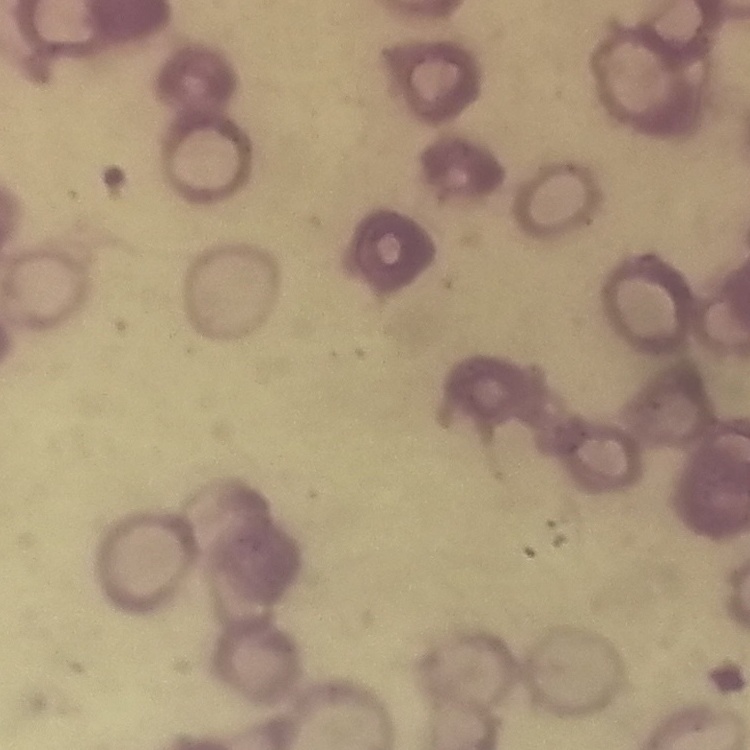

Summary:
  - Erythrocyte morphology: rouleaux formation
  - Image type: square crop of a larger photomicrograph
  - Preparation: thin peripheral smear
  - Stain: Field's or Giemsa